Outline every Plasmodium parasite, every leukocyte, and every artifact (stain precipitate or debris).
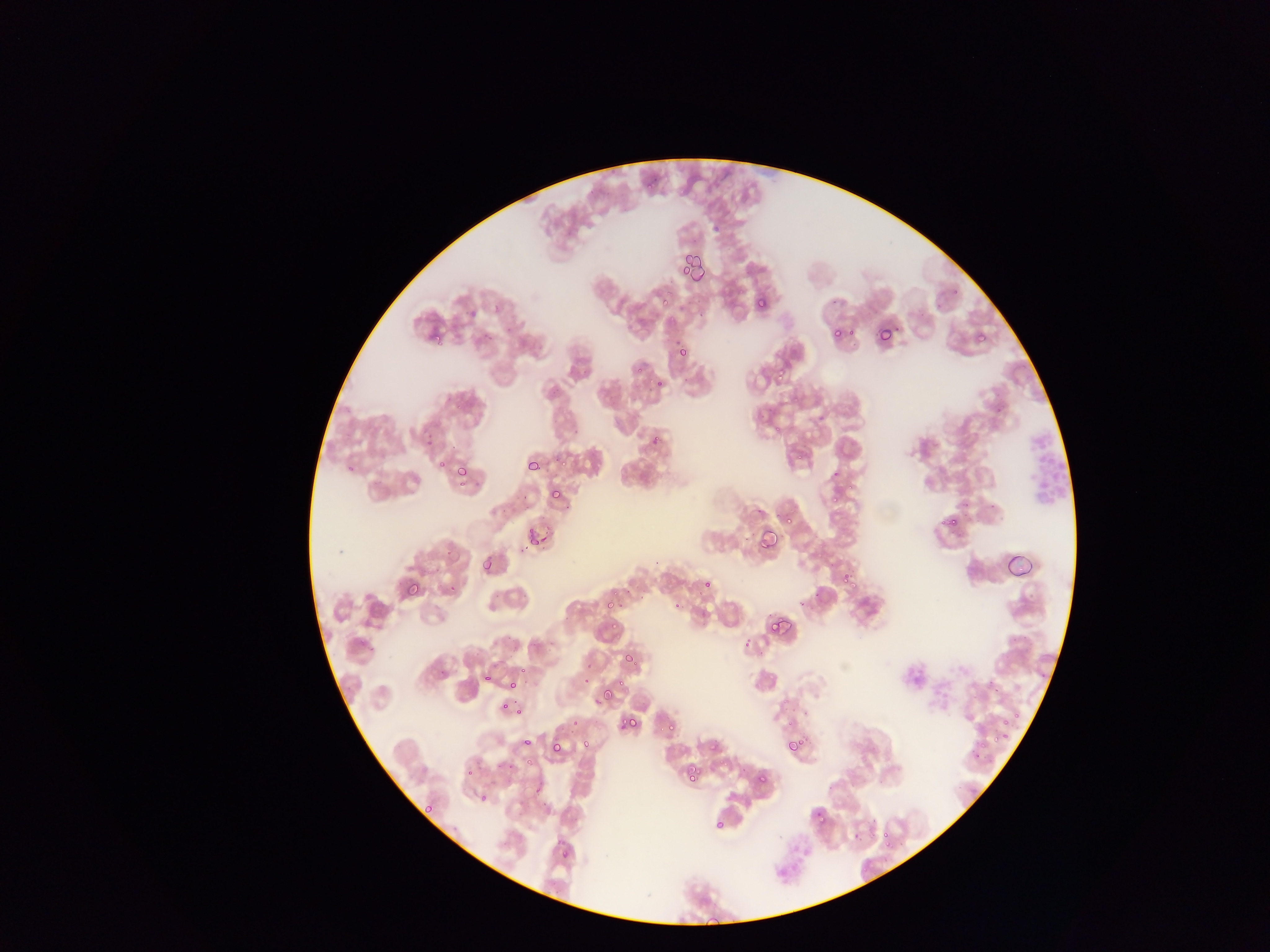

Approximate bounding boxes as (left, top, right, bottom) in pixels.
Plasmodium parasites: (646, 182, 652, 190), (757, 298, 765, 306), (835, 329, 840, 337), (433, 334, 441, 341), (977, 334, 986, 343), (680, 345, 688, 355), (778, 373, 783, 381), (775, 424, 780, 432), (796, 453, 805, 459), (560, 460, 569, 466), (457, 467, 466, 476), (833, 467, 840, 478), (551, 490, 561, 500), (831, 494, 837, 502), (940, 519, 950, 524), (527, 527, 535, 534), (540, 536, 548, 543), (530, 539, 538, 546), (447, 550, 452, 558), (840, 572, 849, 584), (407, 580, 423, 596), (702, 581, 711, 586), (850, 581, 858, 589), (619, 602, 623, 610), (673, 603, 683, 608), (770, 621, 777, 632), (744, 637, 752, 647), (624, 655, 633, 664), (520, 669, 528, 672), (485, 674, 493, 680), (583, 677, 590, 685), (510, 682, 518, 688), (603, 687, 613, 700), (502, 703, 510, 709), (622, 717, 627, 725), (630, 720, 636, 728), (786, 720, 794, 727), (797, 734, 805, 746), (991, 737, 999, 742), (788, 739, 795, 751), (979, 741, 987, 748), (551, 743, 563, 752), (709, 744, 717, 751), (974, 752, 982, 758), (686, 765, 697, 773), (688, 774, 695, 783), (757, 776, 767, 783), (425, 804, 433, 815), (816, 813, 824, 822), (715, 820, 724, 828), (883, 829, 890, 837), (854, 830, 859, 839), (562, 850, 567, 858) | approximate (x, y) pixel centers of objects too small to bound: (685, 269), (665, 302), (852, 332), (639, 370), (659, 383), (657, 438), (442, 464), (350, 469), (461, 485), (789, 521), (954, 521), (452, 589), (628, 591), (616, 594), (610, 606), (614, 626), (636, 662), (443, 672), (621, 683), (518, 711), (1017, 715), (575, 722), (1006, 722), (671, 727), (662, 729), (1005, 737), (527, 741), (585, 744), (529, 761), (511, 766), (470, 773), (483, 796), (887, 844).
No leukocytes observed.

Summary:
  - Country: Ghana
  - Preparation: thin blood smear
  - Field of view: single
  - Capture: mobile-phone photograph through a microscope
  - Image size: 1270×952 pixels